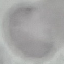
Summary:
  - Result: negative for malaria parasites
  - Stain: Giemsa
  - Capture: smartphone camera at the microscope eyepiece
  - Preparation: thin smear
  - Image type: automatically extracted cell patch, resized to 64 × 64 pixels